Describe the morphology of the erythrocytes.
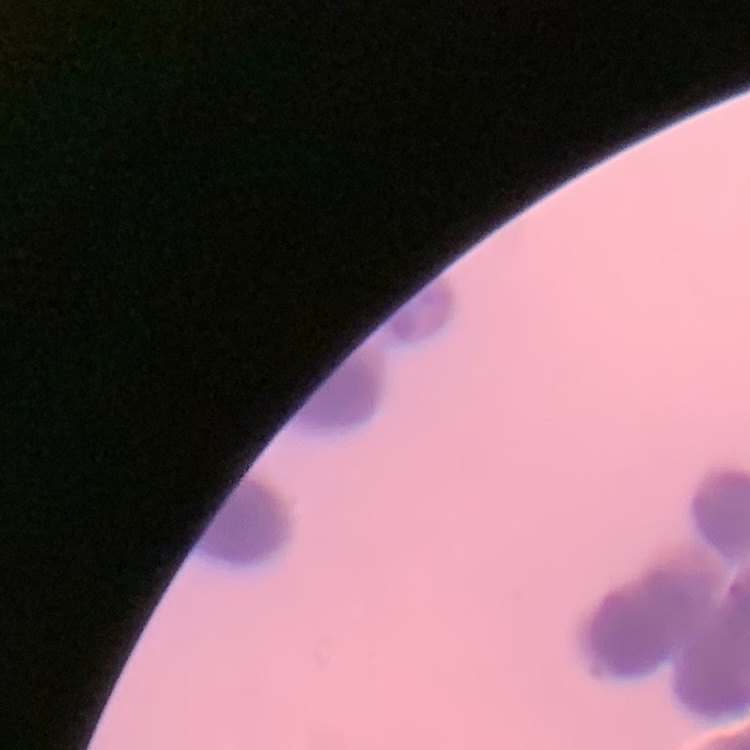

Rouleaux formation.

One tile cut from a larger photomicrograph. Thin peripheral smear. Field's or Giemsa stain.